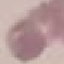

result = negative for malaria parasites
preparation = thin blood smear
image type = automatically extracted cell patch, resized to 64 × 64 pixels
stain = Giemsa
capture = smartphone through the microscope eyepiece